Evaluate for Plasmodium parasites.
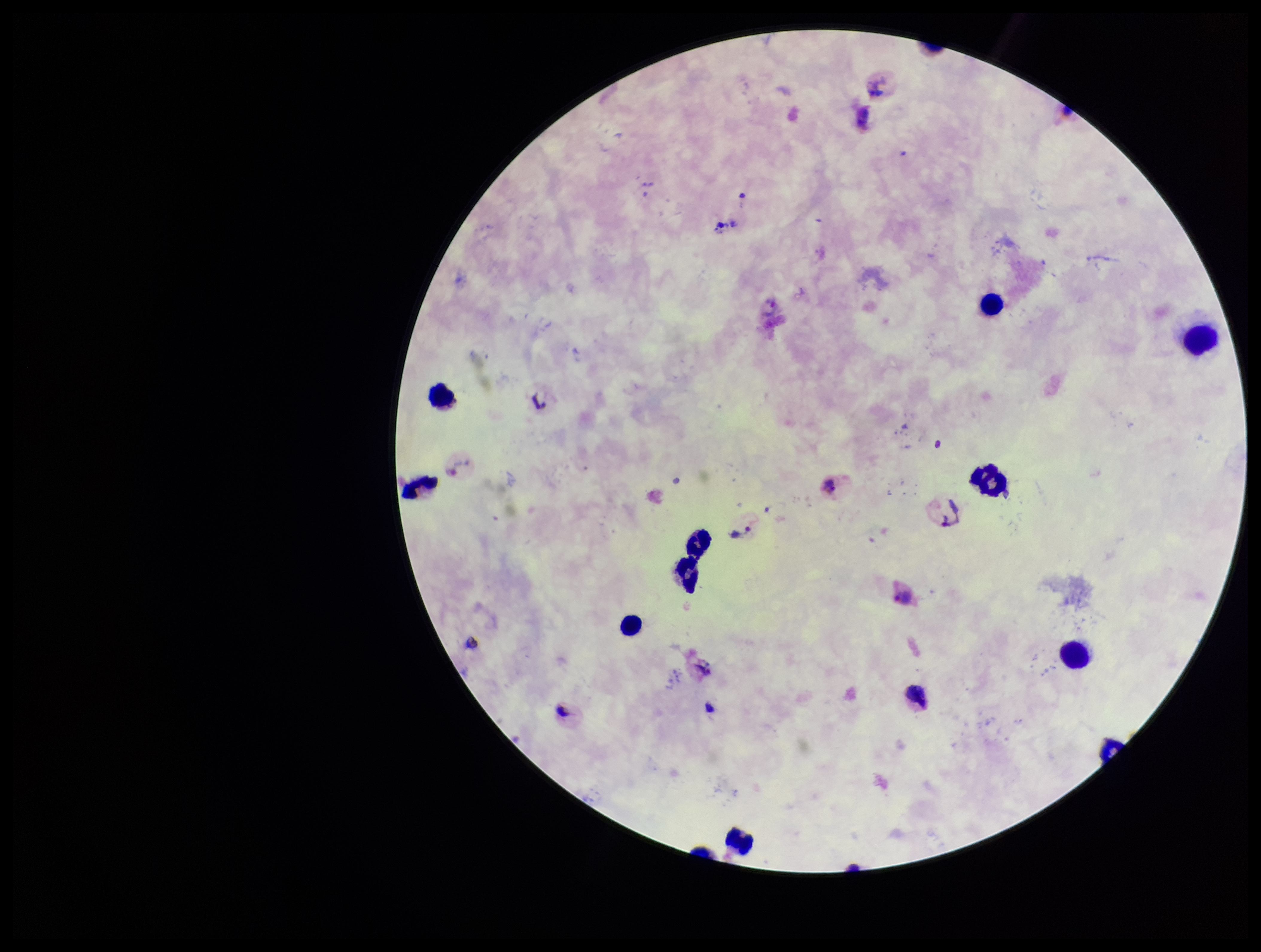

Seen.

{
  "image_size": "1261×952 pixels",
  "preparation": "thick blood smear",
  "field_of_view": "one from this slide",
  "capture": "smartphone photograph through the microscope eyepiece",
  "species_reported_for_this_patient": "Plasmodium vivax",
  "patient_malaria_status": "positive",
  "stain": "Giemsa",
  "leukocyte_count": 10,
  "parasite_count": 4
}